Give the position of every Plasmodium parasite visible.
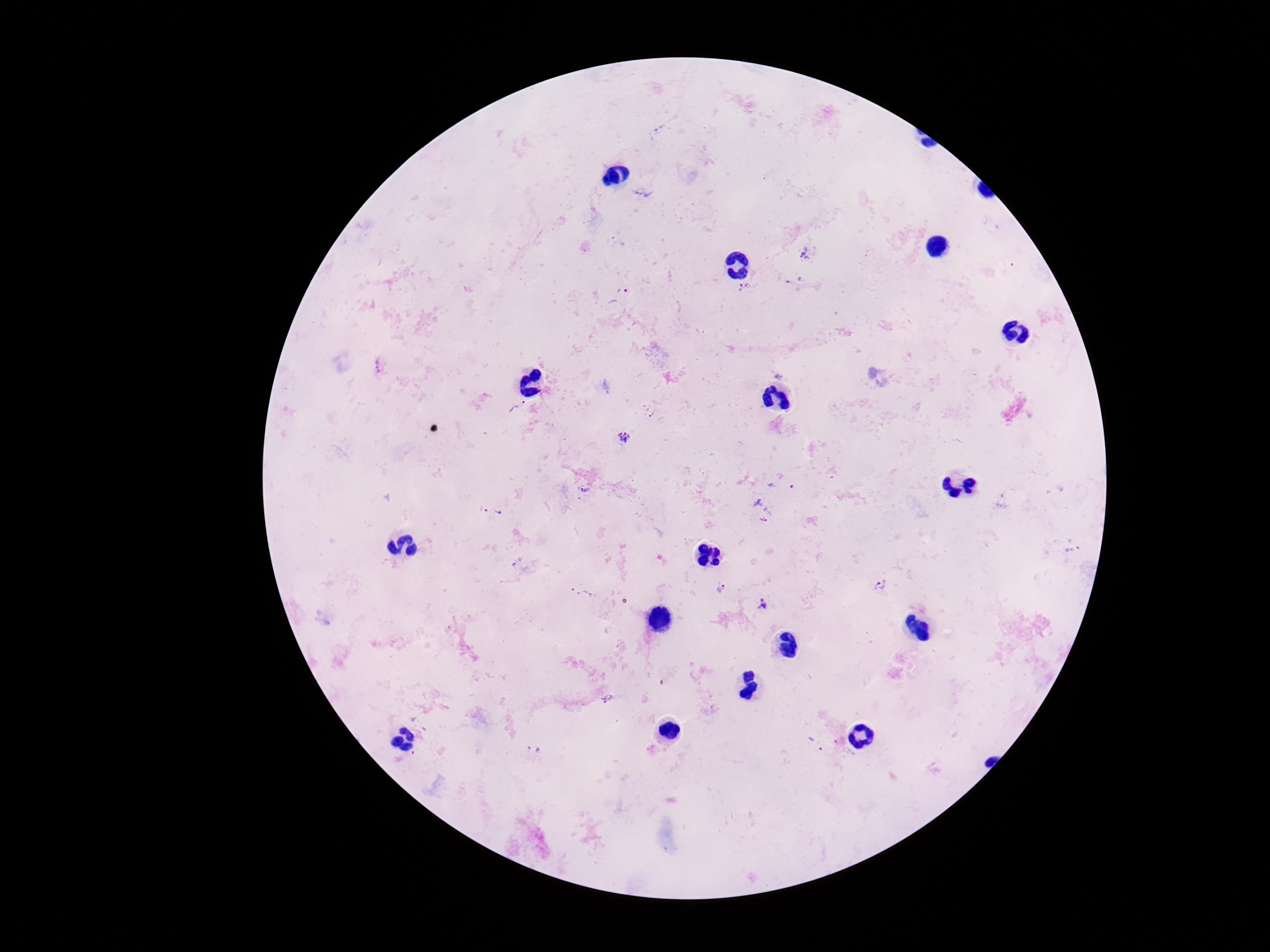

Approximate centers as {x, y} in pixels.
Plasmodium parasites: {659, 131}, {644, 191}, {807, 253}, {795, 281}, {746, 286}, {623, 289}, {379, 367}, {779, 376}, {518, 408}, {649, 411}, {624, 437}, {584, 490}, {1004, 502}, {762, 510}, {492, 511}, {1073, 549}, {879, 585}, {721, 587}, {583, 593}, {764, 607}, {605, 699}, {816, 744}, {534, 751}.

Summary:
  - Magnification: 100x
  - Image size: 1270×952 pixels
  - Field of view: single
  - Capture: smartphone camera through the microscope eyepiece
  - Patient malaria status: infected
  - Preparation: thick blood film
  - Stain: Giemsa